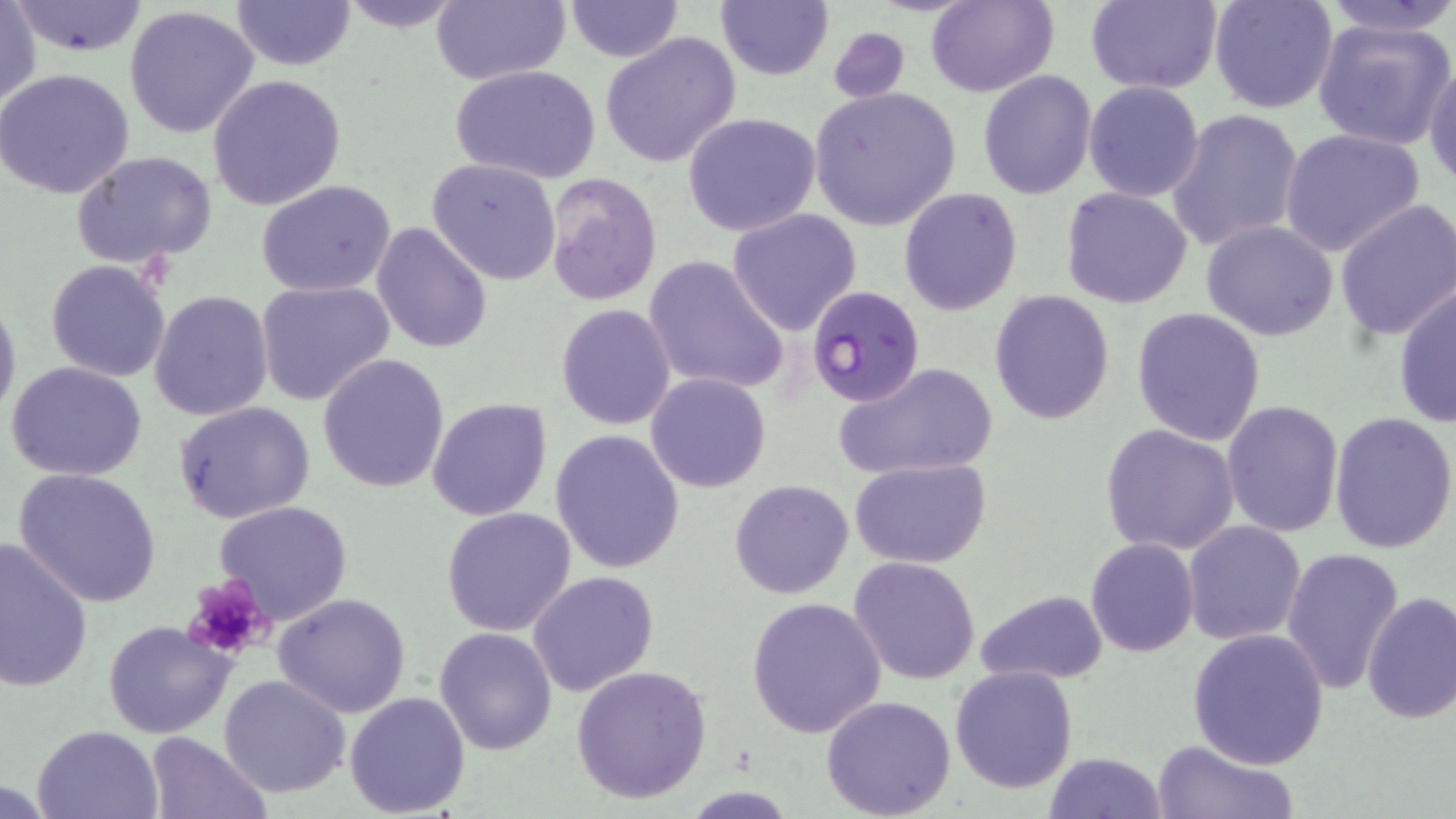
slide-level diagnosis = Plasmodium falciparum
field of view = single
magnification = 1000x
preparation = thin blood film
Plasmodium falciparum-infected red blood cell locations = approximate bounding boxes as (x1,y1)-(x2,y2) corner pairs in pixels: (805,285)-(926,406)
platelet locations = approximate bounding boxes as (x1,y1)-(x2,y2) corner pairs in pixels: (183,575)-(276,659)
image size = 1456×819 pixels
stain = May-Grünwald-Giemsa
modality = optical microscopy
uninfected red blood cell locations = approximate bounding boxes as (x1,y1)-(x2,y2) corner pairs in pixels: (231,0)-(355,71), (335,0)-(465,33), (430,0)-(570,85), (715,0)-(833,81), (1084,0)-(1222,93), (1207,0)-(1339,115), (1315,0)-(1456,39), (11,1)-(152,56), (564,1)-(683,63), (926,1)-(1059,98), (1,2)-(41,110), (123,5)-(261,141), (1312,17)-(1456,149), (826,23)-(910,104), (599,32)-(742,168), (1424,57)-(1456,188), (449,64)-(599,185), (0,67)-(135,198), (977,71)-(1097,200), (207,74)-(348,211), (1083,81)-(1204,202), (809,87)-(961,230), (1166,109)-(1302,253), (681,113)-(822,238), (1279,128)-(1425,258), (71,150)-(219,270), (426,157)-(564,285), (542,172)-(665,306), (256,181)-(398,298), (898,187)-(1022,316), (1061,187)-(1192,308), (1334,199)-(1456,342), (727,209)-(862,335), (1200,220)-(1339,340), (371,222)-(492,355), (642,253)-(791,395), (45,260)-(171,383), (256,280)-(394,408), (1392,285)-(1455,428), (150,290)-(274,422), (988,291)-(1115,427), (0,293)-(21,423), (555,302)-(676,430), (1130,308)-(1265,447), (318,352)-(451,492), (833,361)-(1001,480), (6,363)-(149,480), (645,372)-(770,493), (426,397)-(552,521), (171,400)-(316,524), (1221,400)-(1345,539), (1329,410)-(1456,554), (1099,423)-(1242,556), (549,429)-(686,574), (849,459)-(993,567), (12,467)-(163,607), (729,480)-(855,600), (213,500)-(352,622), (440,507)-(577,636), (1182,521)-(1306,644), (0,537)-(96,694), (1085,537)-(1199,656), (1280,547)-(1403,697), (848,556)-(982,685), (527,571)-(659,696), (974,589)-(1108,686), (1361,591)-(1456,725), (272,592)-(411,718), (745,596)-(887,739), (103,618)-(237,740), (434,626)-(559,755), (1186,628)-(1329,769), (570,664)-(713,805), (949,665)-(1078,794), (219,674)-(351,797), (343,690)-(472,816), (822,695)-(956,817), (33,723)-(163,817), (143,731)-(272,818), (1152,740)-(1297,819), (1043,751)-(1167,818)